Name the parasite shown.
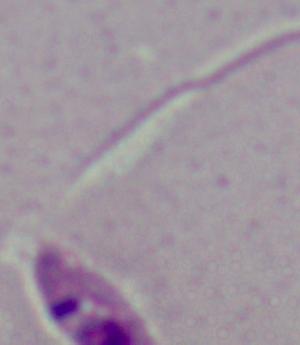

This is Leishmania.

{
  "magnification": "1000x",
  "modality": "micrograph"
}